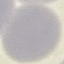 Result: negative for malaria parasites. Thin smear of blood. Automatically extracted cell patch, resized to 64 × 64 pixels. Giemsa-stained preparation. Photographed with a smartphone camera at the microscope eyepiece.